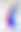
{
  "modality": "micrograph",
  "identification": "Toxoplasma gondii",
  "magnification": "400x"
}